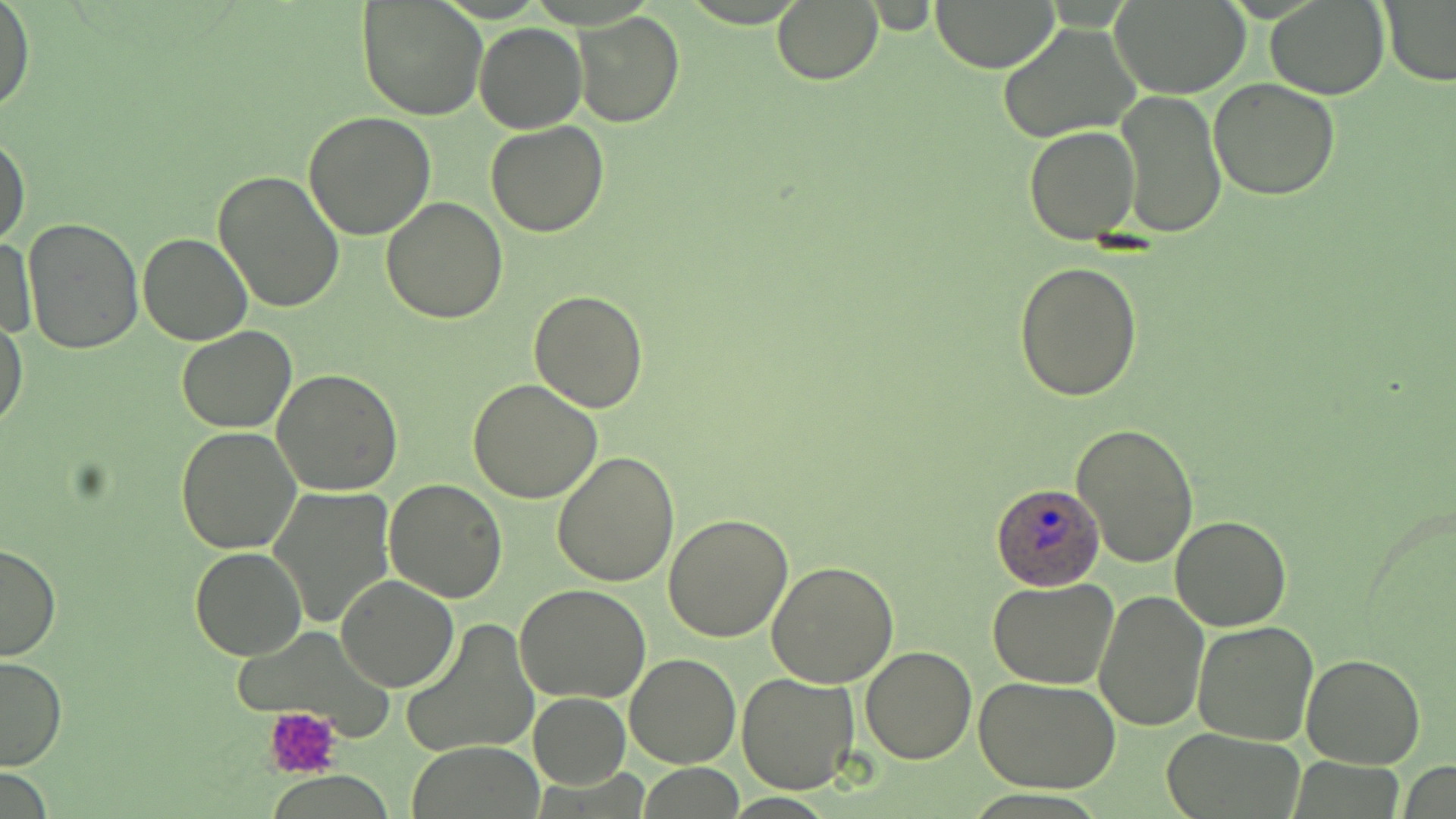
Summary:
  - Coordinate format: approximate bounding boxes as (x1,y1)-(x2,y2) corner pairs in pixels
  - Plasmodium ovale-infected red blood cell locations: (987,482)-(1105,592)
  - Platelet locations: (263,707)-(344,780)
  - Uninfected red blood cell locations: (357,0)-(487,122), (771,0)-(884,86), (931,0)-(1059,71), (1380,0)-(1456,88), (0,1)-(34,114), (1266,1)-(1388,99), (1113,2)-(1250,99), (573,11)-(684,127), (997,22)-(1141,143), (474,23)-(587,134), (1208,77)-(1341,201), (1116,91)-(1225,238), (303,112)-(436,242), (485,122)-(611,237), (1024,125)-(1140,244), (0,130)-(31,247), (212,170)-(345,313), (382,197)-(508,322), (22,219)-(144,354), (138,232)-(251,345), (1,234)-(39,338), (1014,260)-(1144,402), (529,288)-(648,412), (1,318)-(29,430), (176,326)-(298,433), (271,369)-(404,496), (468,378)-(602,503), (1072,422)-(1199,568), (176,426)-(303,554), (551,451)-(679,588), (385,480)-(508,603), (268,486)-(394,628), (663,513)-(794,643), (1169,515)-(1291,630), (0,541)-(61,661), (190,547)-(306,659), (765,561)-(898,686), (336,575)-(457,692), (986,578)-(1117,687), (515,583)-(651,703), (1094,588)-(1208,733), (400,618)-(539,759), (1193,620)-(1319,746), (860,647)-(978,765), (625,653)-(740,767), (1302,653)-(1425,768), (0,655)-(67,772), (735,672)-(858,795), (973,673)-(1121,792), (528,692)-(631,790), (1157,728)-(1306,818), (409,744)-(546,817)
  - Slide-level diagnosis: Plasmodium ovale
  - Image size: 1456×819 pixels
  - Stain: May-Grünwald-Giemsa
  - Field of view: single
  - Preparation: thin blood smear
  - Modality: light microscopy
  - Magnification: 1000x